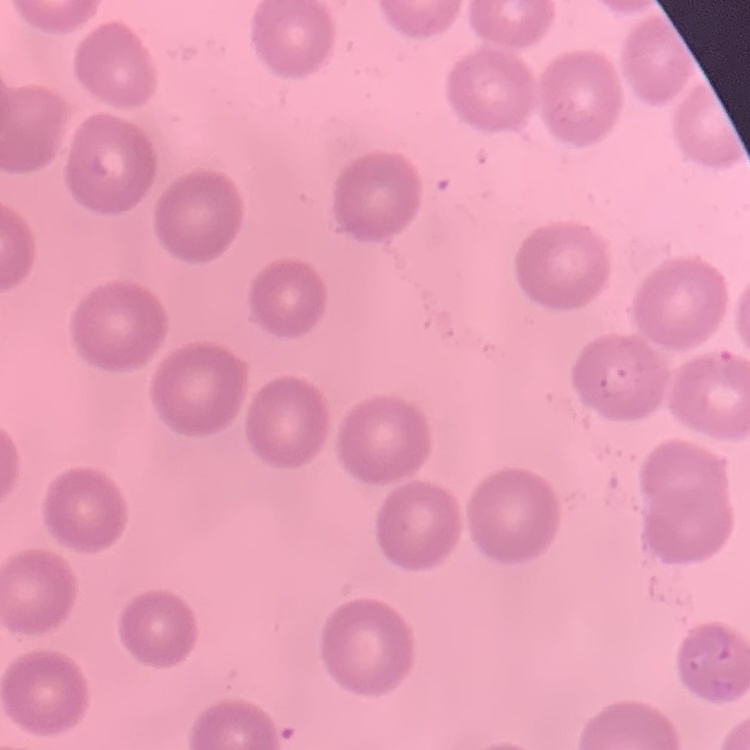
erythrocyte_morphology: no rouleaux formation
preparation: thin blood film
image_type: square crop of a larger photomicrograph
stain: Field's or Giemsa